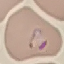 Result: malaria parasites identified. Acquired by smartphone through the microscope eyepiece. Automatically extracted cell patch, resized to 64 × 64 pixels. Giemsa stain. Thin smear of blood.